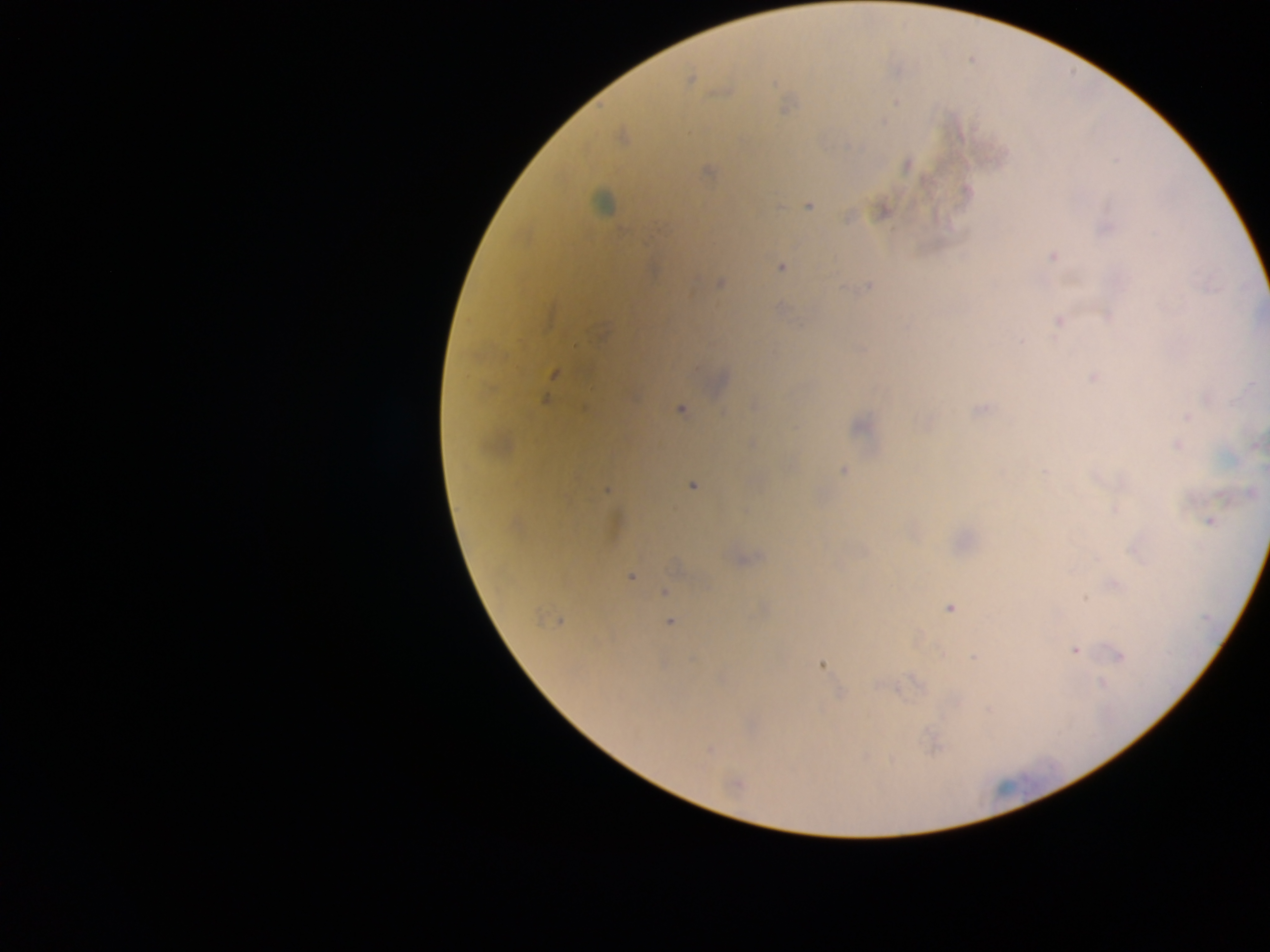
capture = mobile-phone photograph through a microscope
preparation = thick blood smear
field of view = single
image size = 1270×952 pixels
country = Ghana
object labeled both Plasmodium parasite and leukocyte by the source = approximate centers as (x, y) in pixels: (603, 202)
Plasmodium parasite locations = approximate centers as (x, y) in pixels: (691, 79), (895, 102), (883, 121), (622, 135), (906, 164), (967, 192), (809, 205), (883, 211), (1106, 228), (1052, 256), (780, 266), (720, 281), (869, 285), (779, 309), (1109, 316), (1059, 321), (599, 333), (554, 374), (1093, 375), (545, 398), (981, 408), (679, 409), (1186, 417), (926, 423), (860, 426), (751, 442), (1178, 444), (1255, 445), (843, 470), (1044, 471), (692, 484), (606, 489), (1251, 493), (1116, 509), (1210, 521), (743, 560), (676, 565), (630, 576), (1113, 583), (665, 593), (1084, 598), (948, 607), (763, 608), (557, 622), (669, 622), (1075, 650), (1117, 655), (974, 658), (820, 663), (957, 700), (989, 710), (709, 749), (736, 783)